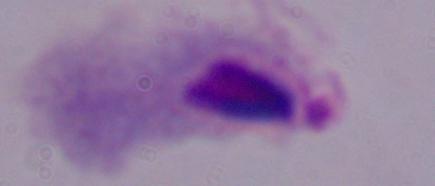 A trichomonad is seen. 1000x magnification. Micrograph.